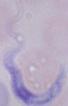
magnification = 1000x
identification = trypanosome
modality = photomicrograph